State which parasite is depicted.
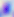
This is Toxoplasma gondii.

magnification = 400x
modality = photomicrograph